Outline each blood parasite and name the species.
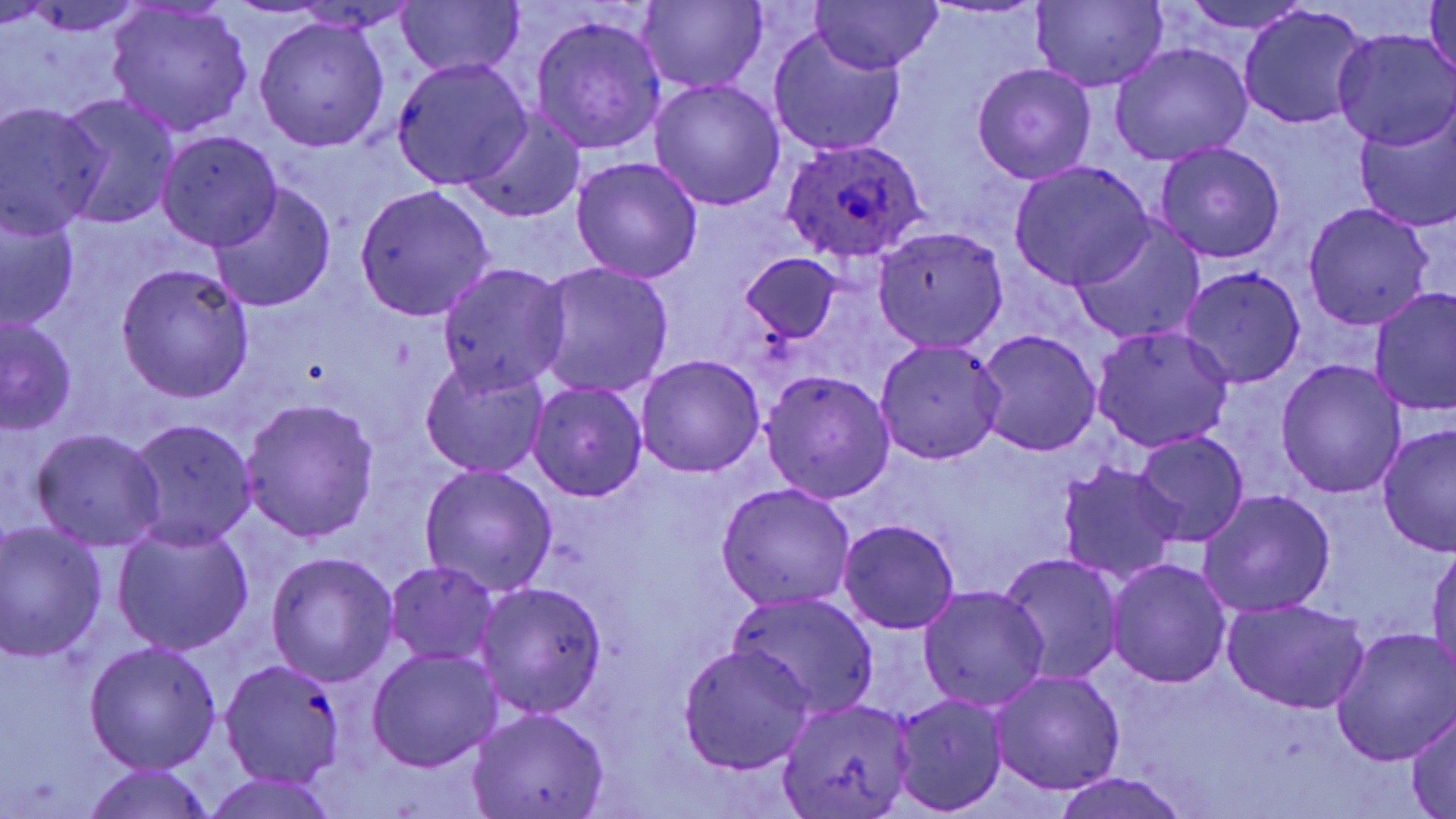

Approximate bounding boxes as (x1, y1, x2, y2) in pixels.
Plasmodium ovale-infected red blood cells: (782, 138, 927, 263).
No Plasmodium falciparum, Plasmodium malariae, Plasmodium vivax, Babesia divergens, or Trypanosoma brucei observed.

Summary:
  - Uninfected red blood cell locations: (810, 0, 940, 74), (1031, 0, 1168, 92), (1177, 0, 1314, 35), (1425, 0, 1456, 84), (395, 1, 522, 79), (634, 1, 768, 90), (105, 5, 254, 138), (1238, 7, 1370, 128), (531, 14, 666, 154), (254, 17, 389, 152), (768, 27, 906, 158), (1333, 30, 1456, 149), (1109, 43, 1251, 165), (392, 58, 532, 190), (972, 63, 1097, 184), (649, 78, 785, 211), (57, 94, 180, 228), (0, 106, 108, 235), (1354, 106, 1456, 236), (461, 110, 587, 224), (158, 130, 282, 250), (1155, 141, 1285, 264), (571, 157, 703, 284), (1011, 162, 1154, 289), (208, 184, 335, 313), (355, 185, 495, 322), (1304, 203, 1433, 329), (0, 209, 79, 332), (1070, 217, 1204, 345), (873, 227, 1008, 353), (743, 253, 842, 342), (437, 263, 570, 393), (537, 263, 675, 400), (116, 264, 254, 402), (1180, 266, 1305, 387), (1370, 286, 1456, 417), (1, 316, 77, 433), (1093, 325, 1234, 452), (975, 329, 1102, 456), (875, 339, 1007, 464), (635, 355, 765, 479), (1276, 359, 1405, 499), (419, 360, 550, 478), (761, 371, 894, 503), (527, 381, 646, 503), (239, 397, 379, 545), (127, 419, 257, 548), (1376, 424, 1456, 557), (30, 429, 167, 551), (1134, 432, 1250, 546), (1057, 462, 1185, 585), (418, 465, 558, 596), (716, 482, 857, 610), (1199, 490, 1335, 617), (837, 518, 961, 634), (1, 523, 107, 662), (112, 523, 254, 656), (1428, 547, 1456, 677), (266, 551, 398, 685), (999, 554, 1122, 683), (1106, 558, 1231, 689), (384, 561, 498, 665), (475, 582, 608, 719), (918, 585, 1049, 712), (729, 592, 880, 719), (1222, 599, 1371, 715), (1329, 628, 1455, 766), (84, 641, 222, 775), (677, 643, 817, 776), (366, 648, 502, 772), (217, 658, 348, 789), (989, 669, 1125, 795), (890, 694, 1008, 817), (775, 699, 916, 818), (467, 707, 610, 819), (1407, 708, 1455, 818), (80, 766, 219, 819), (1049, 773, 1193, 819), (198, 774, 346, 819)
  - Slide-level diagnosis: Plasmodium ovale
  - Modality: light microscopy
  - Field of view: single
  - Image size: 1456×819 pixels
  - Preparation: thin blood film
  - Stain: May-Grünwald-Giemsa
  - Magnification: 1000x